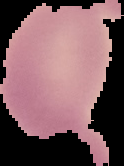

{
  "preparation": "thin blood film",
  "image_size": "124×166 pixels",
  "malaria_status": "uninfected",
  "image_type": "segmented cell region on a black background"
}